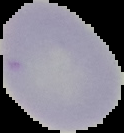

Malaria status: uninfected. Cell region segmented out of the field of view; the surrounding area is masked to black. From a thin blood smear. Image is 124×133 pixels.